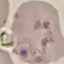
Summary:
  - Result: no malaria parasites detected
  - Stain: Giemsa
  - Preparation: thin smear
  - Capture: smartphone camera at the microscope eyepiece
  - Image type: automatically extracted cell patch, resized to 64 × 64 pixels